Locate every blood parasite and identify its species.
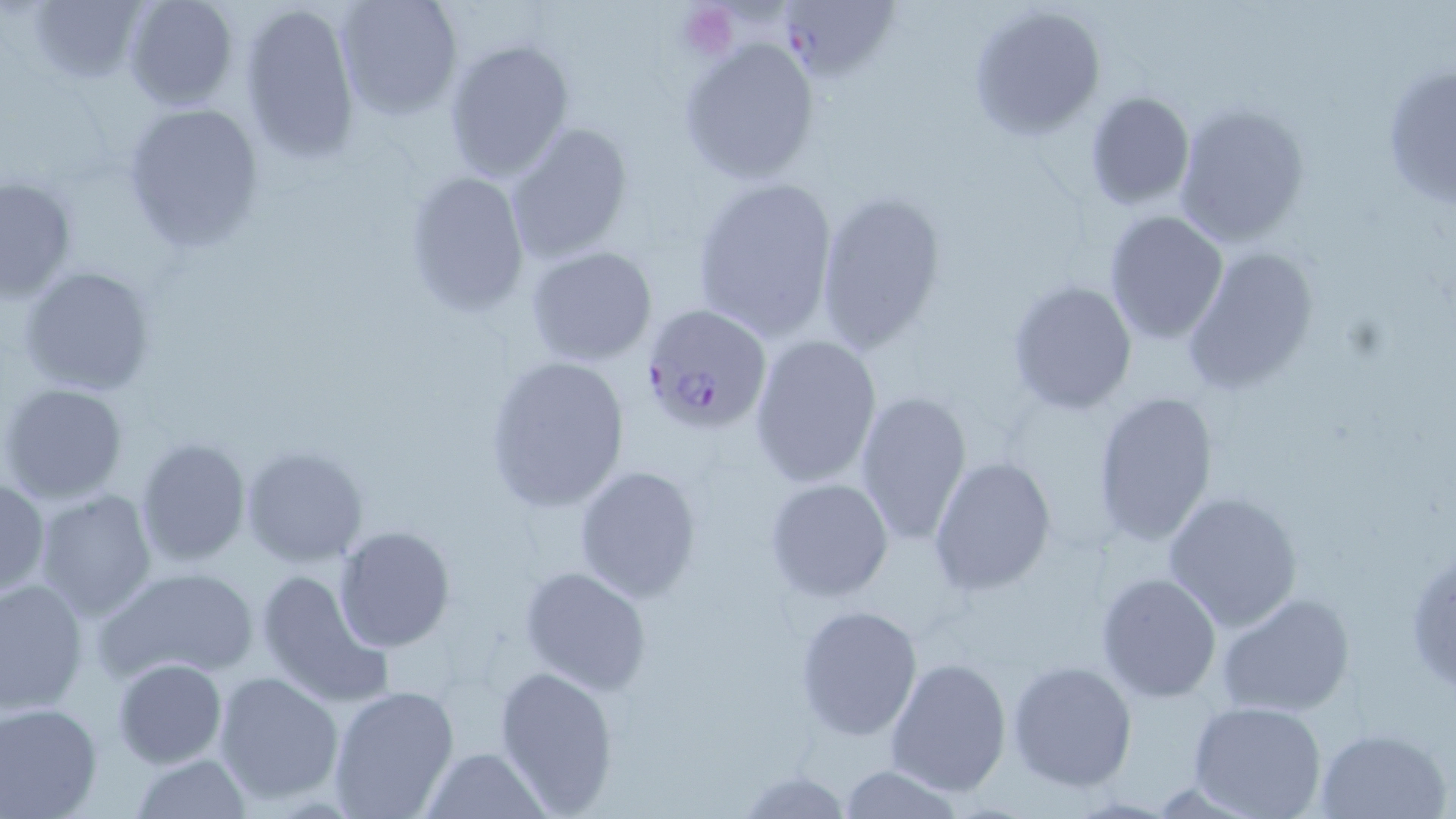
Approximate bounding boxes as (x1, y1, x2, y2) in pixels.
Plasmodium falciparum-infected red blood cells: (784, 5, 902, 88), (642, 304, 773, 432).
No Plasmodium ovale, Plasmodium malariae, Plasmodium vivax, Babesia divergens, or Trypanosoma brucei observed.

Summary:
  - Platelet locations: (678, 5, 736, 56)
  - Uninfected red blood cell locations: (26, 0, 148, 87), (121, 0, 241, 110), (333, 0, 463, 119), (239, 2, 362, 162), (968, 4, 1105, 139), (679, 35, 821, 185), (443, 39, 574, 182), (1380, 59, 1455, 214), (1083, 90, 1196, 211), (1172, 101, 1312, 248), (121, 102, 266, 254), (506, 121, 635, 262), (402, 170, 530, 316), (691, 173, 840, 340), (0, 174, 76, 301), (813, 191, 948, 356), (1104, 209, 1229, 343), (1181, 244, 1319, 394), (525, 245, 658, 366), (20, 266, 155, 396), (1006, 279, 1136, 414), (750, 334, 883, 486), (481, 354, 630, 515), (1, 382, 127, 504), (853, 388, 974, 546), (1092, 389, 1218, 548), (133, 436, 252, 568), (241, 443, 369, 566), (929, 456, 1058, 594), (574, 465, 702, 601), (0, 477, 48, 598), (764, 478, 896, 602), (33, 489, 158, 621), (1161, 489, 1302, 631), (333, 525, 456, 652), (1406, 542, 1456, 700), (519, 565, 652, 695), (94, 566, 259, 687), (254, 567, 393, 708), (1097, 572, 1222, 703), (0, 578, 88, 717), (1215, 593, 1355, 717), (794, 603, 925, 741), (885, 656, 1012, 797), (113, 658, 227, 769), (1007, 659, 1137, 792), (495, 665, 619, 814), (214, 670, 343, 806), (326, 684, 460, 818), (1189, 700, 1328, 819), (0, 701, 103, 818), (1313, 725, 1450, 818), (422, 747, 548, 819), (132, 754, 253, 817), (837, 764, 967, 818), (736, 768, 852, 817)
  - Slide-level diagnosis: Plasmodium falciparum
  - Image size: 1456×819 pixels
  - Modality: light microscopy
  - Field of view: single
  - Stain: May-Grünwald-Giemsa
  - Magnification: 1000x
  - Preparation: thin blood film